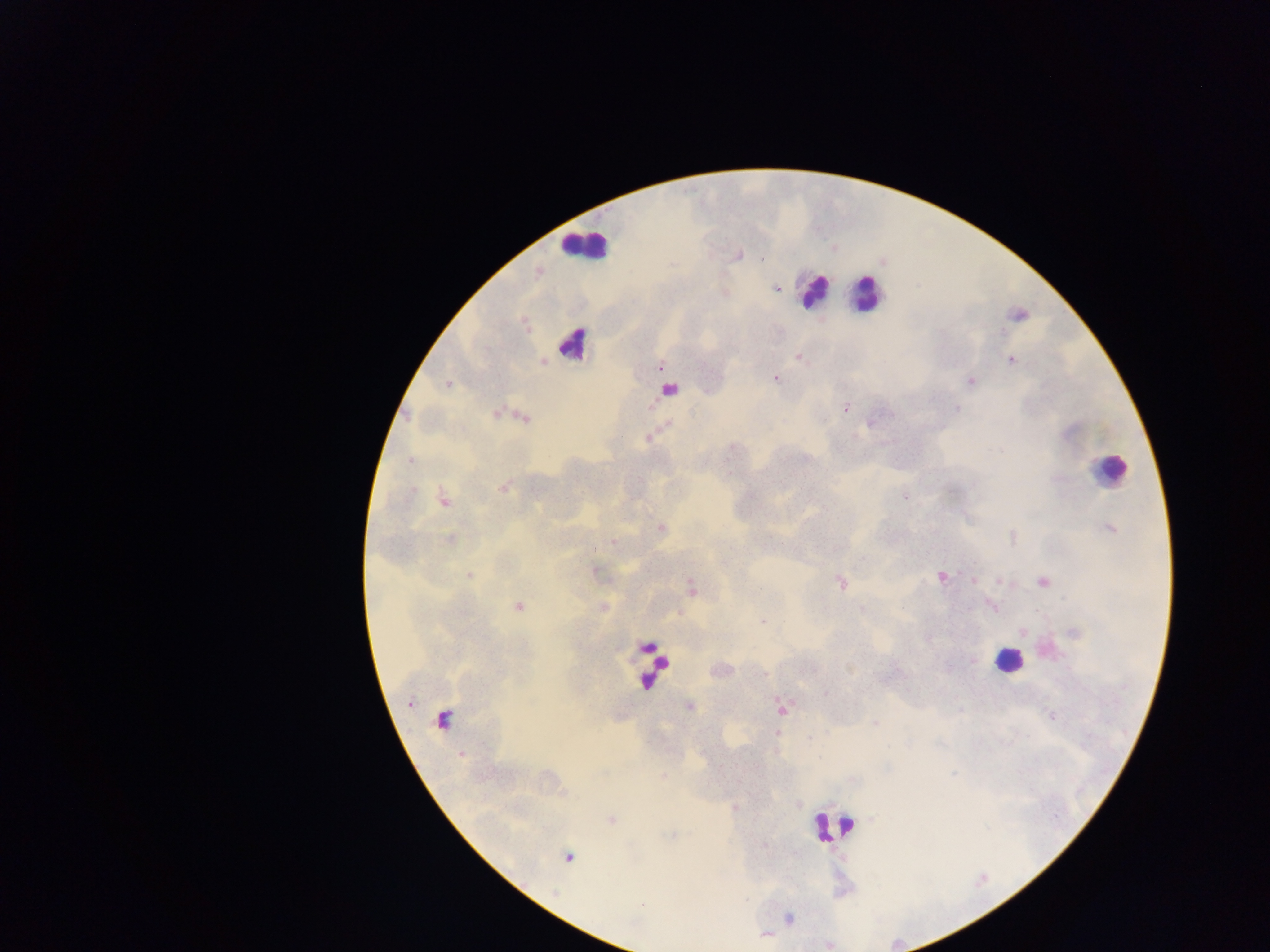
country = Ghana
Plasmodium parasite locations = approximate centers as [x, y] in pixels: [762, 258], [778, 288], [797, 356], [1012, 360], [660, 368], [775, 378], [971, 382], [447, 384], [845, 408], [957, 409], [496, 413], [407, 417], [410, 460], [503, 489], [904, 497], [443, 499], [1110, 528], [661, 529], [1013, 537], [450, 539], [614, 542], [594, 570], [469, 575], [941, 577], [974, 581], [841, 582], [1000, 582], [1042, 582], [519, 606], [991, 607], [763, 621], [973, 660], [825, 693], [410, 703], [689, 706], [782, 709], [1051, 715], [875, 723], [776, 733], [810, 739], [461, 754], [664, 776], [611, 820], [569, 857], [642, 904], [789, 918]
leukocyte locations = approximate centers as [x, y] in pixels: [583, 247], [813, 291], [866, 293], [573, 344], [666, 391], [1108, 469], [1008, 661], [653, 665], [443, 723], [831, 826]
preparation = thick blood smear
capture = mobile-phone photograph through a microscope
field of view = single
image size = 1270×952 pixels